State which parasite is depicted.
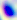

Toxoplasma gondii.

magnification = 400x
modality = micrograph